Assess the morphology of the red blood cells.
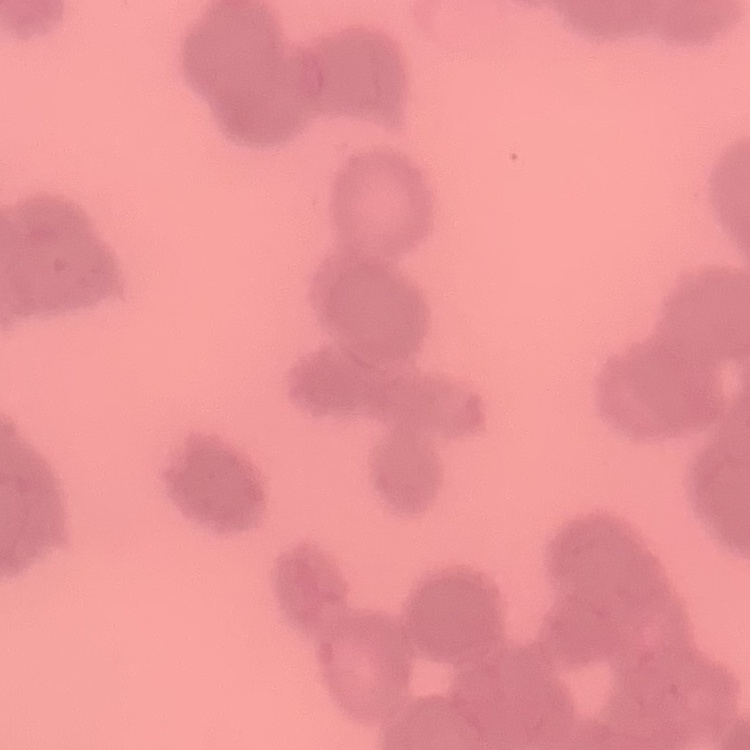

Rouleaux formation.

Thin peripheral smear. Stained with either Field's or Giemsa. Square crop of a larger photomicrograph.